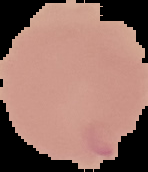

preparation: thin blood film
image_type: cell region segmented out of the field of view; surrounding area masked to black
result: Plasmodium parasites identified
image_size: 148×172 pixels